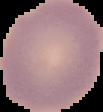 From a thin blood smear. Cell region segmented out of the field of view; the surrounding area is masked to black. Malaria status: uninfected. Image is 103×112 pixels.